State the blood parasite species.
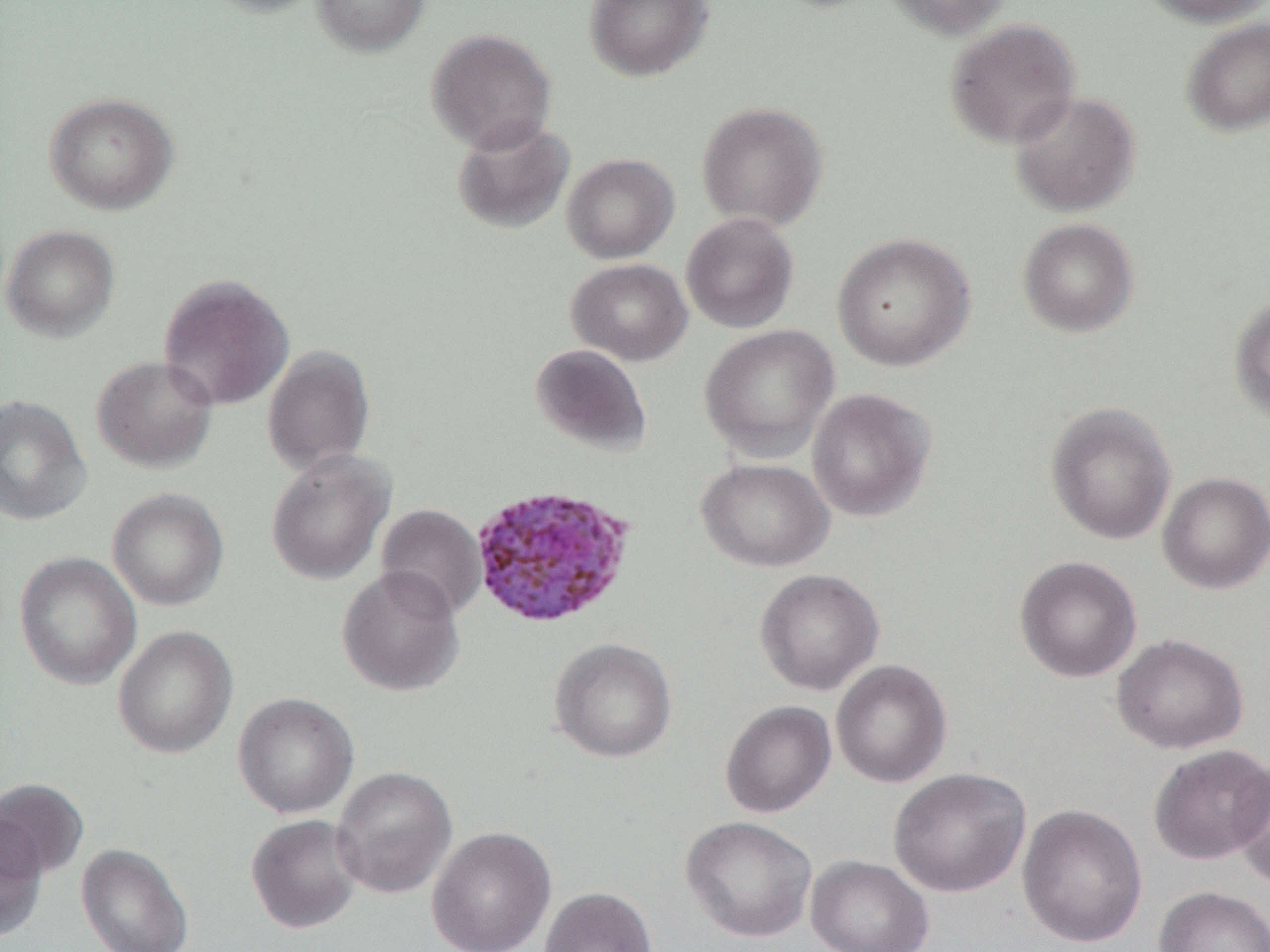

Plasmodium ovale.

Approximate bounding boxes as [x1, y1, x2, y2] in pixels. Uninfected red blood cell locations: [201, 0, 327, 18], [312, 0, 430, 56], [584, 0, 713, 81], [880, 0, 1014, 39], [1140, 0, 1269, 26], [1181, 17, 1270, 136], [944, 18, 1081, 149], [427, 27, 557, 153], [1009, 90, 1140, 217], [44, 92, 178, 215], [697, 101, 828, 231], [451, 118, 574, 235], [562, 153, 679, 263], [681, 212, 799, 333], [1017, 218, 1139, 337], [1, 225, 120, 341], [832, 232, 976, 371], [567, 258, 693, 365], [158, 273, 294, 411], [1230, 293, 1270, 426], [698, 325, 839, 461], [262, 344, 376, 475], [530, 344, 652, 457], [91, 355, 218, 472], [806, 387, 936, 522], [0, 394, 91, 525], [1045, 402, 1176, 545], [266, 449, 395, 585], [697, 457, 834, 572], [1157, 472, 1270, 594], [107, 488, 229, 610], [375, 503, 486, 619], [14, 551, 142, 690], [1014, 555, 1142, 683], [337, 565, 465, 696], [755, 568, 885, 695], [113, 625, 238, 759], [1111, 633, 1249, 754], [549, 637, 677, 763], [831, 659, 952, 788], [233, 693, 359, 818], [720, 700, 836, 818], [1148, 744, 1270, 865], [1230, 763, 1270, 889], [331, 765, 458, 899], [888, 767, 1031, 897], [0, 778, 89, 881], [1017, 803, 1147, 948], [246, 813, 365, 934], [0, 814, 47, 940], [680, 815, 818, 943], [426, 826, 556, 952], [75, 843, 194, 952], [806, 854, 933, 952], [1153, 885, 1270, 952], [539, 886, 657, 952]. Plasmodium ovale-infected red blood cell locations: [469, 483, 636, 629]. Optical microscopy. Image is 1270×952 pixels. One field of a larger specimen. Thin blood film. Captured at 1000x magnification.